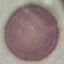

Summary:
  - Malaria status: uninfected
  - Image type: automatically extracted cell patch, resized to 64 × 64 pixels
  - Capture: smartphone camera at the microscope eyepiece
  - Stain: Giemsa
  - Preparation: thin smear